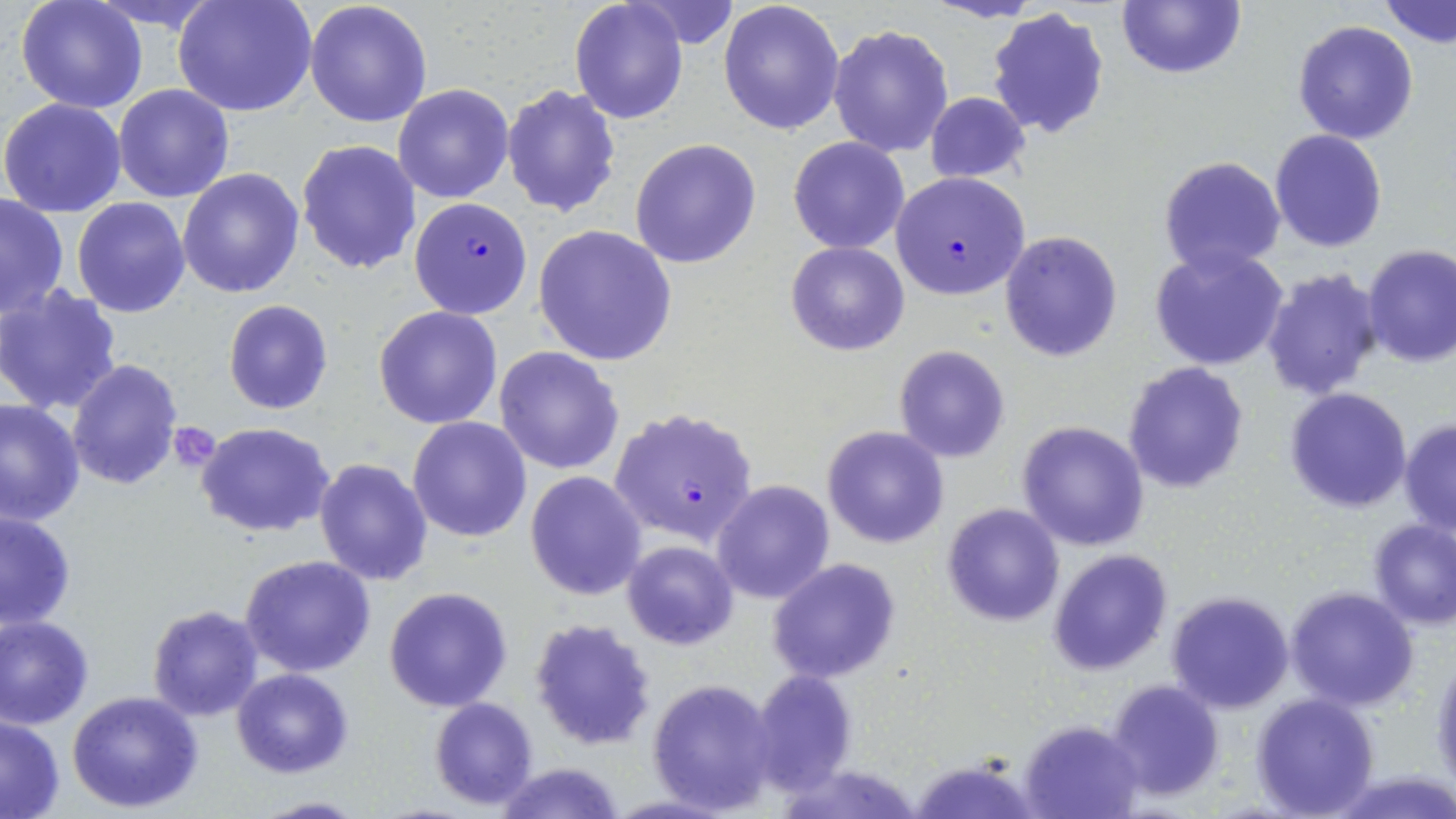
Plasmodium falciparum-infected red blood cell locations = approximate bounding boxes as [x1, y1, x2, y2] in pixels: [890, 172, 1031, 301], [409, 197, 531, 320], [611, 409, 758, 546]
slide-level diagnosis = Plasmodium falciparum
magnification = 1000x
platelet locations = approximate bounding boxes as [x1, y1, x2, y2] in pixels: [166, 422, 222, 472]
field of view = single
preparation = thin blood film
uninfected red blood cell locations = approximate bounding boxes as [x1, y1, x2, y2] in pixels: [173, 0, 317, 119], [718, 0, 845, 137], [1116, 0, 1246, 81], [16, 1, 148, 113], [305, 1, 434, 128], [569, 1, 689, 122], [1381, 1, 1456, 47], [986, 7, 1109, 140], [1292, 19, 1420, 145], [828, 24, 953, 158], [392, 83, 515, 203], [114, 84, 234, 203], [502, 84, 620, 217], [924, 91, 1030, 185], [0, 98, 127, 219], [1269, 129, 1387, 252], [788, 137, 909, 253], [630, 138, 762, 269], [297, 140, 421, 274], [1158, 155, 1287, 276], [178, 168, 305, 298], [0, 194, 69, 317], [72, 196, 192, 317], [534, 224, 678, 367], [1000, 231, 1123, 361], [786, 241, 910, 355], [1149, 245, 1291, 372], [1362, 245, 1456, 366], [1260, 266, 1387, 399], [0, 284, 124, 417], [223, 299, 333, 415], [374, 305, 502, 429], [894, 345, 1011, 463], [494, 346, 623, 474], [66, 358, 184, 490], [1122, 362, 1250, 495], [1284, 387, 1413, 514], [0, 397, 85, 525], [407, 416, 532, 542], [1398, 418, 1455, 537], [1016, 420, 1150, 553], [194, 422, 336, 537], [822, 425, 949, 549], [313, 458, 434, 587], [525, 471, 648, 600], [712, 480, 834, 603], [942, 502, 1066, 627], [1, 509, 76, 633], [1366, 517, 1455, 631], [622, 540, 739, 650], [1048, 549, 1173, 675], [240, 555, 377, 678], [767, 558, 901, 684], [383, 586, 513, 712], [1285, 587, 1418, 711], [1165, 591, 1293, 713], [145, 604, 264, 721], [0, 614, 95, 729], [529, 617, 656, 751], [1430, 652, 1455, 793], [748, 667, 858, 795], [232, 668, 354, 778], [649, 678, 779, 812], [1105, 679, 1225, 802], [66, 689, 204, 812], [1249, 691, 1380, 818], [429, 696, 540, 809], [0, 715, 66, 817], [1020, 720, 1143, 818], [905, 753, 1037, 819], [493, 762, 627, 819], [248, 795, 371, 817]
stain = May-Grünwald-Giemsa
modality = light microscopy
image size = 1456×819 pixels